Outline each Plasmodium malariae-infected red blood cell.
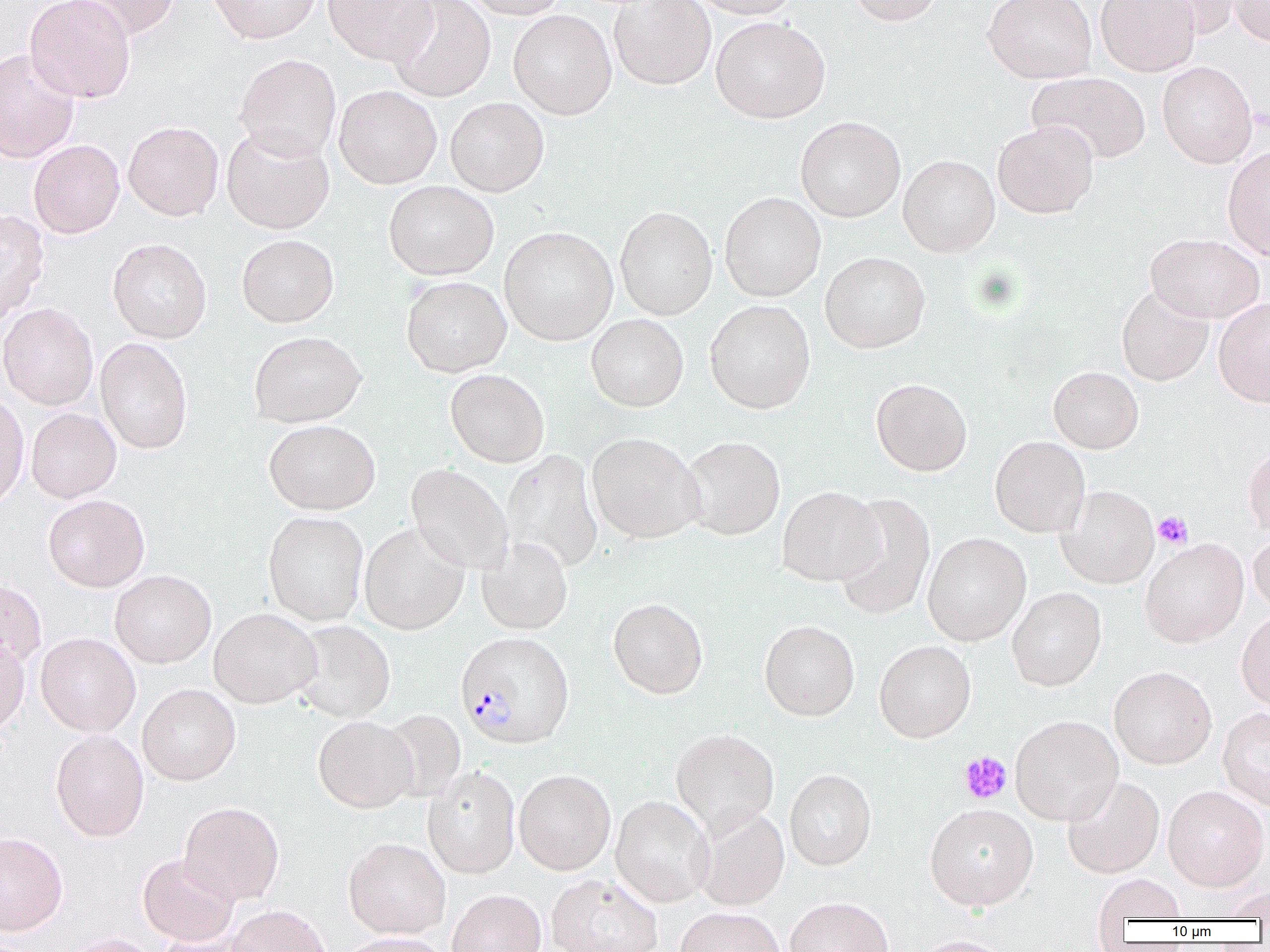
Approximate bounding boxes as [x1, y1, x2, y2] in pixels.
Plasmodium malariae-infected red blood cells: [455, 631, 573, 749].

{
  "slide_level_diagnosis": "Plasmodium malariae",
  "image_size": "1270×952 pixels",
  "modality": "light microscopy",
  "uninfected_red_blood_cell_locations": "approximate bounding boxes as [x1, y1, x2, y2] in pixels: [24, 0, 135, 102], [66, 0, 181, 41], [208, 0, 323, 44], [323, 0, 439, 66], [389, 0, 496, 102], [460, 0, 568, 19], [609, 0, 717, 90], [686, 0, 801, 18], [848, 0, 944, 26], [983, 0, 1097, 83], [1095, 0, 1200, 76], [1143, 0, 1244, 39], [1229, 0, 1270, 46], [508, 9, 617, 119], [710, 16, 831, 124], [0, 49, 80, 163], [234, 53, 341, 161], [1157, 61, 1258, 168], [1027, 71, 1151, 164], [334, 85, 442, 189], [445, 97, 549, 196], [795, 116, 906, 222], [992, 120, 1099, 219], [123, 121, 224, 221], [221, 124, 335, 234], [28, 139, 125, 238], [1222, 145, 1270, 260], [898, 154, 1000, 257], [384, 180, 499, 280], [719, 192, 826, 302], [614, 206, 718, 320], [0, 210, 50, 323], [498, 226, 618, 345], [1145, 233, 1265, 323], [237, 234, 339, 327], [108, 238, 212, 343], [820, 251, 931, 353], [401, 276, 511, 377], [1116, 285, 1214, 386], [1213, 296, 1270, 407], [705, 300, 815, 414], [0, 303, 99, 409], [586, 314, 688, 412], [248, 330, 366, 427], [95, 337, 193, 454], [1048, 366, 1144, 453], [445, 369, 550, 467], [871, 378, 973, 476], [0, 392, 29, 511], [26, 408, 121, 503], [264, 419, 381, 515], [586, 432, 705, 543], [681, 435, 786, 540], [990, 436, 1090, 538], [1243, 444, 1270, 538], [500, 449, 604, 573], [406, 463, 512, 575], [1056, 485, 1159, 588], [777, 486, 884, 586], [832, 492, 936, 620], [43, 494, 150, 592], [263, 511, 368, 625], [359, 522, 468, 635], [923, 532, 1031, 645], [1248, 532, 1270, 614], [477, 536, 573, 635], [1140, 538, 1249, 648], [109, 570, 216, 668], [0, 578, 46, 671], [1007, 587, 1106, 691], [608, 597, 708, 699], [208, 608, 321, 708], [1236, 609, 1270, 711], [290, 620, 396, 723], [759, 620, 860, 721], [35, 633, 140, 737], [0, 634, 30, 735], [874, 640, 976, 742], [1109, 666, 1217, 769], [137, 684, 241, 785], [1217, 707, 1270, 810], [379, 709, 465, 803], [1010, 715, 1123, 825], [313, 716, 417, 812], [670, 728, 780, 834], [50, 729, 149, 842], [423, 767, 520, 878], [784, 769, 876, 870], [514, 770, 615, 875], [1062, 775, 1164, 879], [1163, 785, 1269, 891], [610, 796, 713, 907], [178, 802, 284, 905], [925, 803, 1038, 909], [692, 806, 790, 911], [0, 832, 68, 935], [343, 837, 451, 938], [137, 854, 239, 947], [546, 873, 663, 952], [1093, 874, 1186, 924], [1217, 886, 1270, 920], [447, 889, 546, 952], [784, 897, 893, 952], [226, 905, 331, 952], [675, 907, 786, 952], [58, 933, 160, 952], [336, 933, 453, 952], [912, 935, 1014, 952]",
  "magnification": "1000x",
  "platelet_locations": "approximate bounding boxes as [x1, y1, x2, y2] in pixels: [1153, 511, 1193, 549], [958, 751, 1013, 804]",
  "preparation": "thin blood smear",
  "field_of_view": "one of a larger specimen"
}